Locate every Plasmodium falciparum-infected red blood cell.
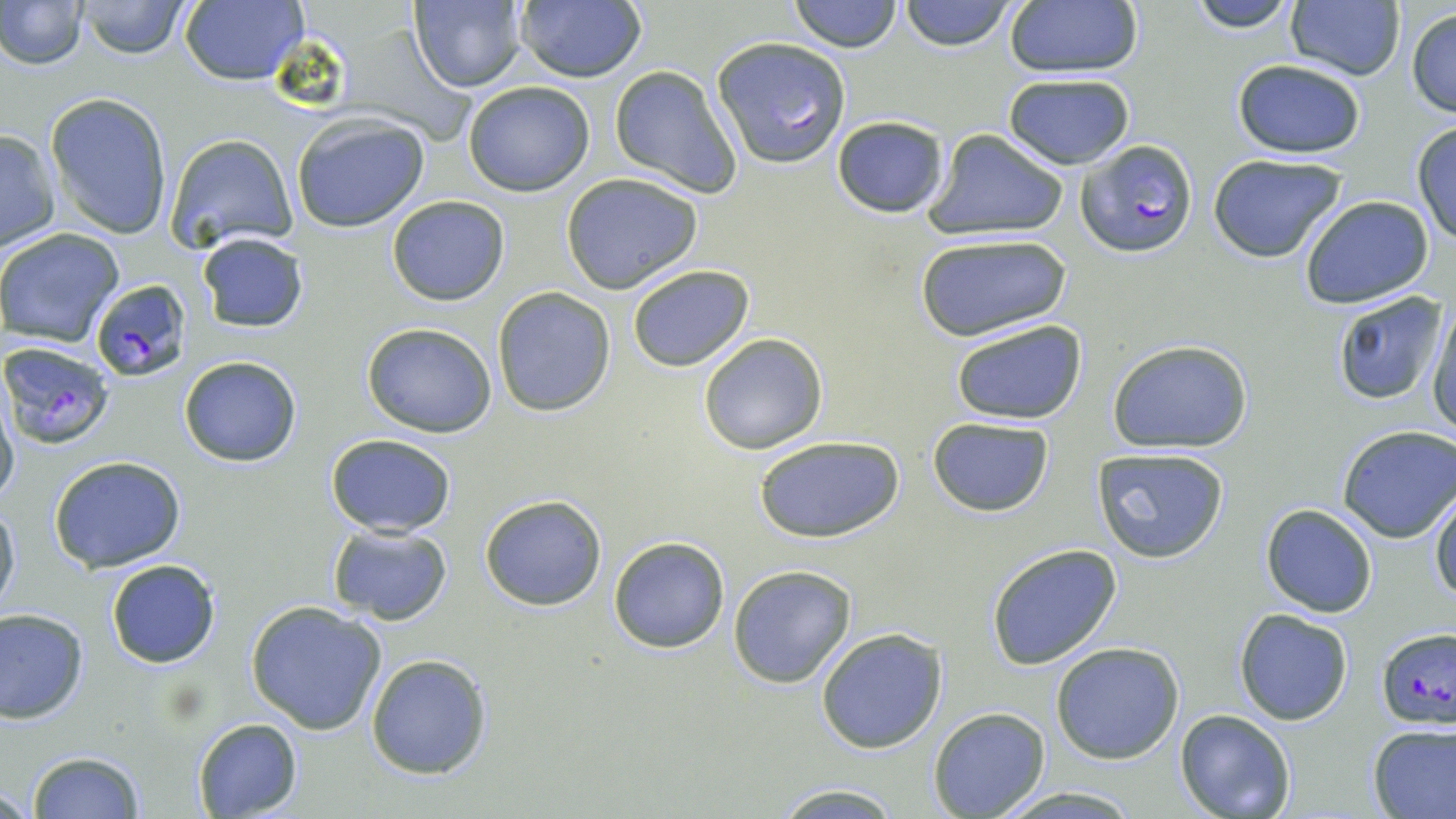
Approximate bounding boxes as (x1,y1)-(x2,y2) corner pairs in pixels.
Plasmodium falciparum-infected red blood cells: (1075,138)-(1198,259), (90,279)-(191,382), (3,341)-(116,449), (1374,627)-(1456,732).

slide-level diagnosis = Plasmodium falciparum
uninfected red blood cell locations = approximate bounding boxes as (x1,y1)-(x2,y2) corner pairs in pixels: (1,0)-(88,69), (74,0)-(196,58), (179,0)-(307,85), (409,0)-(528,94), (513,0)-(646,84), (787,0)-(903,54), (896,0)-(1019,52), (1184,0)-(1302,33), (1283,0)-(1404,82), (1001,2)-(1145,79), (1406,6)-(1455,120), (711,37)-(851,168), (1229,59)-(1367,158), (607,66)-(740,198), (1001,72)-(1137,169), (462,80)-(595,196), (45,92)-(173,241), (832,115)-(949,219), (291,116)-(430,233), (1411,120)-(1456,244), (0,129)-(59,250), (925,130)-(1068,240), (165,133)-(299,253), (1205,151)-(1348,263), (560,172)-(704,294), (386,196)-(509,305), (1300,196)-(1435,308), (0,227)-(123,348), (197,232)-(308,333), (915,234)-(1070,342), (626,263)-(754,372), (492,288)-(616,415), (1331,290)-(1446,406), (1425,297)-(1456,438), (951,317)-(1087,426), (362,321)-(498,437), (697,333)-(827,455), (1107,340)-(1253,454), (178,354)-(302,466), (0,388)-(19,511), (925,417)-(1056,517), (1337,425)-(1456,541), (324,432)-(457,537), (753,433)-(905,544), (1091,446)-(1230,565), (47,455)-(189,572), (1430,489)-(1456,606), (478,493)-(606,610), (0,498)-(20,618), (1260,503)-(1378,617), (325,522)-(453,625), (609,536)-(730,654), (985,542)-(1123,670), (105,559)-(221,669), (727,564)-(856,687), (244,602)-(388,736), (0,607)-(89,723), (1234,608)-(1354,725), (816,628)-(948,754), (1048,642)-(1187,764), (366,654)-(492,777), (928,706)-(1049,818), (1175,710)-(1295,819), (192,717)-(302,818), (1367,723)-(1456,819), (27,751)-(143,818), (770,782)-(909,818), (991,786)-(1144,817)
modality = light microscopy
image size = 1456×819 pixels
field of view = one of a larger specimen
magnification = 1000x
preparation = thin blood film
stain = May-Grünwald-Giemsa